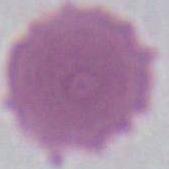
modality: photomicrograph
identification: red blood cell
magnification: 1000x